Name the malaria species.
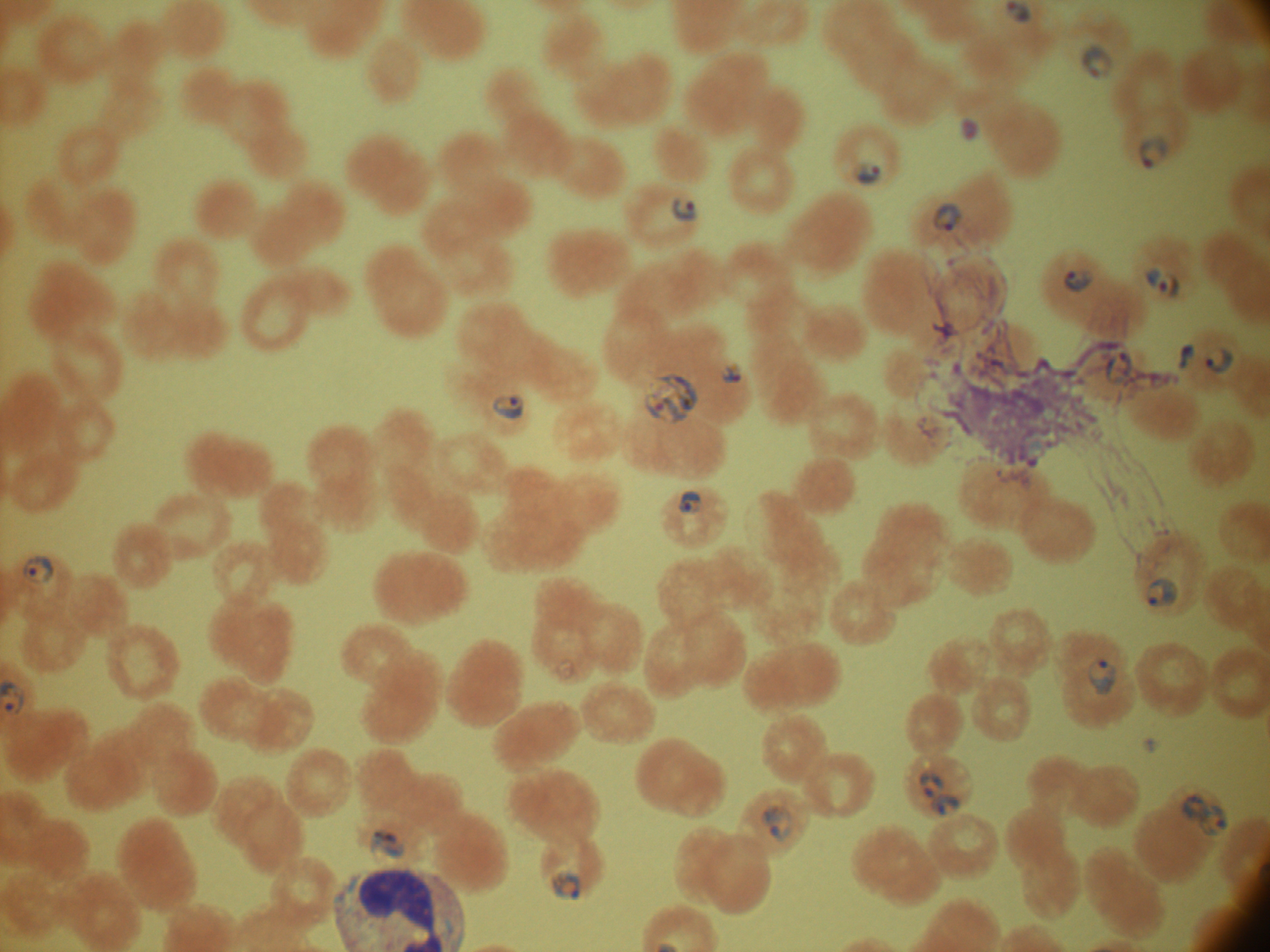

Plasmodium falciparum.

Approximate bounding boxes as named x1/y1/x2/y2 corners in pixels, from the source annotation, which is not necessarily exhaustive. Trophozoite locations: (x1=644, y1=373, x2=699, y2=424). Ring form locations: (x1=1080, y1=43, x2=1113, y2=80), (x1=959, y1=118, x2=980, y2=140), (x1=1139, y1=134, x2=1169, y2=169), (x1=852, y1=161, x2=883, y2=186), (x1=672, y1=197, x2=697, y2=222), (x1=934, y1=202, x2=962, y2=232), (x1=1145, y1=266, x2=1181, y2=298), (x1=1063, y1=269, x2=1095, y2=292), (x1=1177, y1=342, x2=1196, y2=370), (x1=1205, y1=345, x2=1235, y2=374), (x1=722, y1=363, x2=743, y2=384), (x1=493, y1=395, x2=524, y2=421), (x1=678, y1=490, x2=703, y2=515), (x1=22, y1=556, x2=53, y2=585), (x1=1148, y1=577, x2=1179, y2=607), (x1=1088, y1=655, x2=1118, y2=695), (x1=919, y1=769, x2=947, y2=799), (x1=930, y1=789, x2=962, y2=819), (x1=1181, y1=794, x2=1206, y2=822), (x1=1196, y1=802, x2=1230, y2=838), (x1=760, y1=804, x2=793, y2=842), (x1=368, y1=830, x2=407, y2=859), (x1=550, y1=869, x2=581, y2=902). Life-cycle stages among the annotated parasites: ring form, trophozoite. Captured at 100x magnification. Giemsa stain. Image is 1270×952 pixels. Thin blood film. Single field of view. Leica DM2000 optical microscope with a built-in camera.